Mark where platelets are.
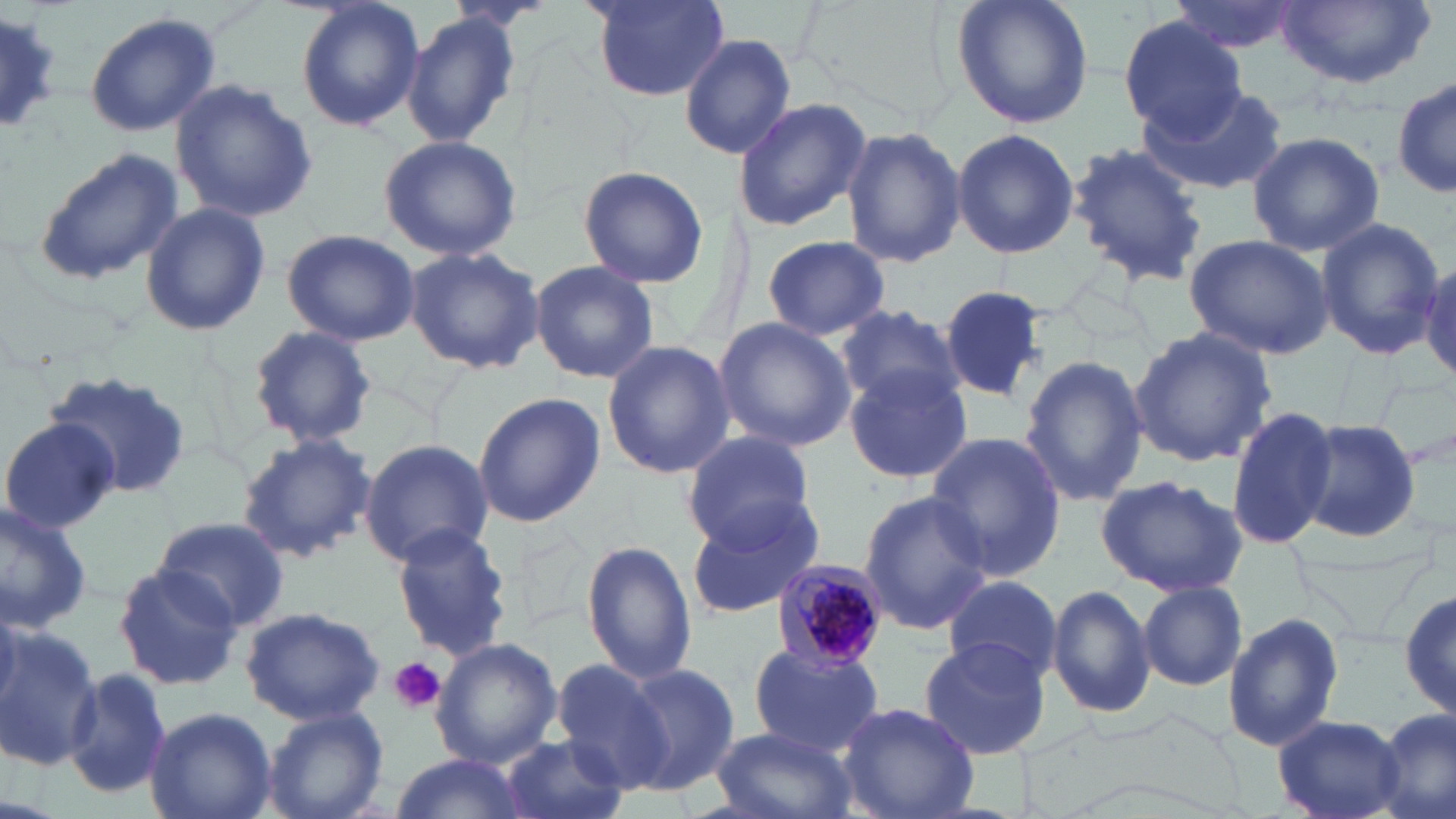
Approximate bounding boxes as (x1, y1, x2, y2) in pixels.
Platelets: (389, 658, 446, 715).

{
  "slide_level_diagnosis": "Plasmodium malariae",
  "magnification": "1000x",
  "preparation": "thin blood film",
  "stain": "May-Grünwald-Giemsa",
  "field_of_view": "single",
  "uninfected_red_blood_cell_locations": "approximate bounding boxes as (x1, y1, x2, y2) in pixels: (293, 0, 424, 134), (590, 0, 731, 102), (950, 0, 1094, 130), (1272, 0, 1434, 89), (1162, 1, 1305, 55), (402, 11, 521, 149), (83, 13, 224, 138), (1119, 13, 1247, 142), (679, 33, 796, 160), (1390, 70, 1453, 204), (169, 79, 319, 222), (1133, 81, 1287, 195), (733, 96, 870, 232), (841, 125, 966, 268), (950, 126, 1079, 260), (1246, 130, 1386, 256), (377, 134, 523, 262), (1066, 142, 1208, 289), (32, 148, 185, 288), (579, 166, 709, 288), (140, 202, 270, 336), (1311, 216, 1446, 360), (282, 228, 420, 347), (1183, 233, 1333, 358), (761, 234, 891, 341), (404, 246, 545, 374), (1418, 250, 1455, 387), (528, 261, 660, 386), (937, 284, 1050, 402), (839, 304, 964, 408), (713, 316, 855, 452), (247, 324, 376, 447), (1128, 326, 1279, 467), (601, 340, 735, 479), (1020, 355, 1147, 506), (844, 364, 974, 485), (44, 372, 195, 505), (472, 391, 605, 529), (1227, 406, 1342, 548), (0, 418, 122, 533), (1298, 421, 1425, 542), (234, 431, 376, 563), (681, 432, 814, 547), (925, 432, 1065, 583), (359, 439, 494, 566), (1097, 474, 1248, 597), (857, 489, 993, 635), (684, 496, 829, 618), (0, 501, 94, 633), (154, 515, 291, 631), (389, 524, 514, 659), (583, 539, 697, 684), (113, 561, 241, 693), (943, 577, 1062, 679), (1138, 582, 1248, 691), (1047, 584, 1156, 720), (1398, 587, 1454, 725), (240, 604, 387, 726), (1223, 611, 1345, 753), (0, 623, 103, 770), (916, 638, 1053, 760), (432, 639, 561, 767), (747, 645, 884, 755), (551, 659, 672, 789), (615, 663, 739, 794), (64, 667, 175, 798), (837, 701, 980, 819), (146, 705, 277, 819), (261, 706, 389, 819), (1374, 709, 1455, 819), (1273, 716, 1405, 818), (711, 726, 858, 819), (499, 736, 629, 819), (386, 754, 531, 819)",
  "plasmodium_malariae_infected_red_blood_cell_locations": "approximate bounding boxes as (x1, y1, x2, y2) in pixels: (772, 559, 889, 670)",
  "modality": "optical microscopy",
  "image_size": "1456×819 pixels"
}